Comment on the morphology of the erythrocytes.
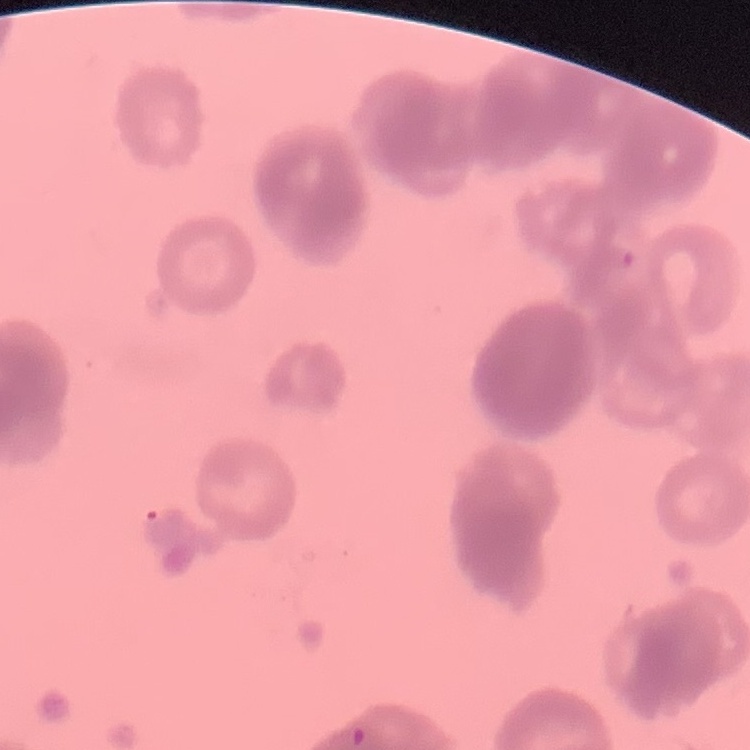
They show rouleaux formation.

Summary:
  - Preparation: thin blood smear
  - Stain: Field's or Giemsa
  - Image type: one tile cut from a larger photomicrograph